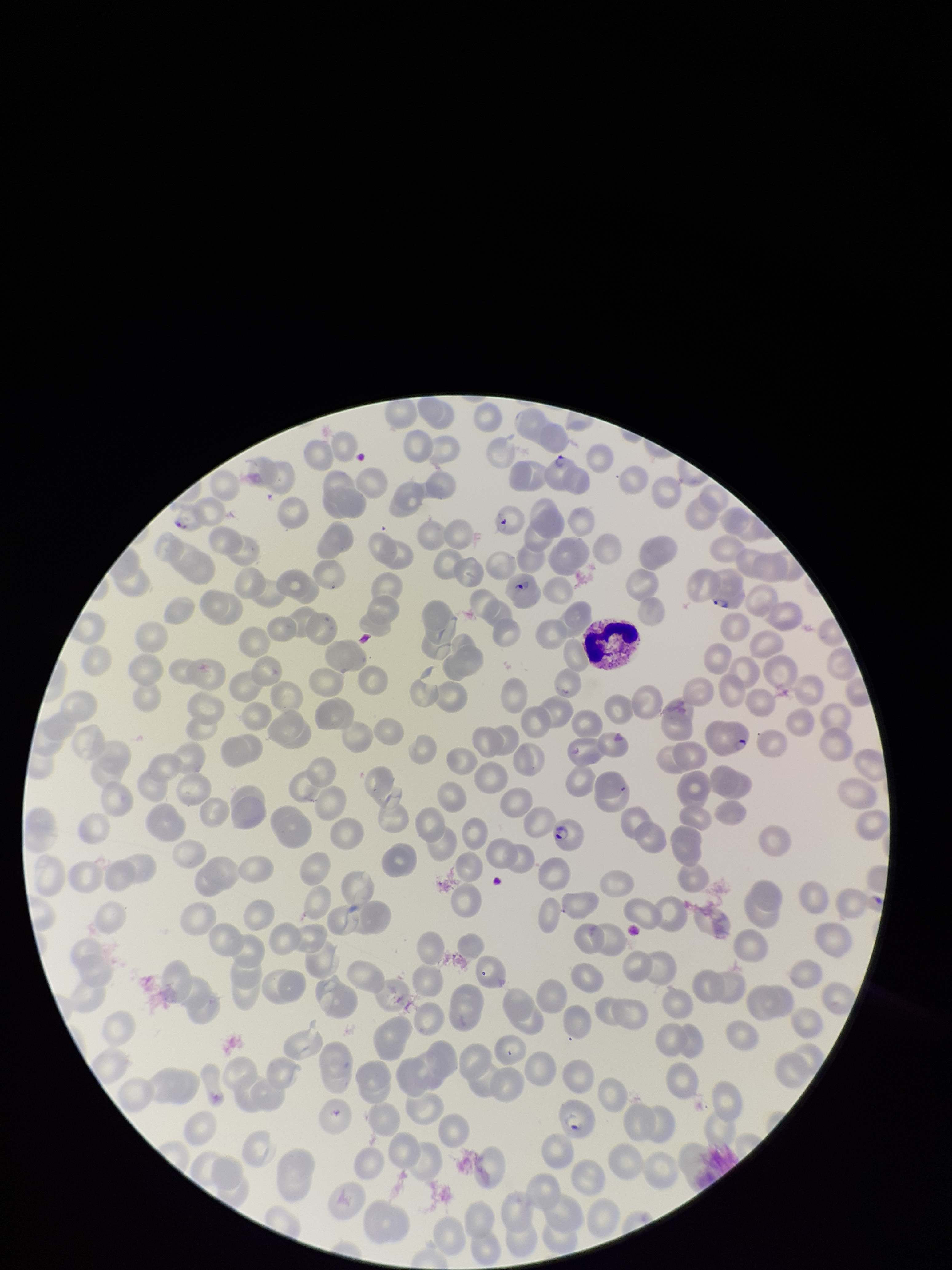
Summary:
  - Species reported for this patient: Plasmodium falciparum
  - Red blood cell count: 214
  - Parasitized red blood cells: detected
  - Stain: Giemsa
  - Patient malaria status: positive
  - Image size: 952×1270 pixels
  - Capture: smartphone photograph through the microscope eyepiece
  - Field of view: one from this slide
  - Preparation: thin smear
  - Parasitized red blood cell count: 7